Comment on the morphology of the red blood cells.
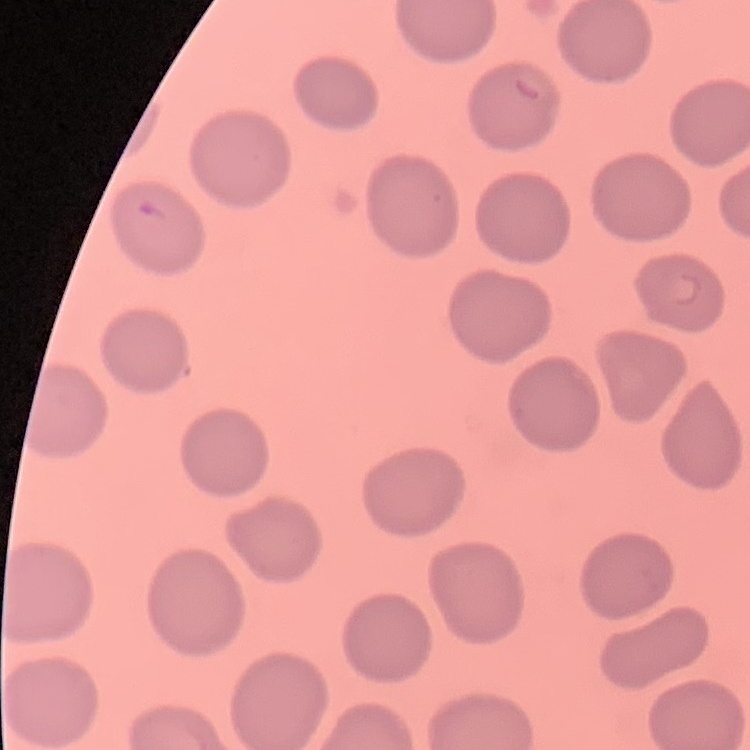

No rouleaux formation.

stain = Field's or Giemsa
preparation = thin peripheral smear
image type = square crop of a larger photomicrograph